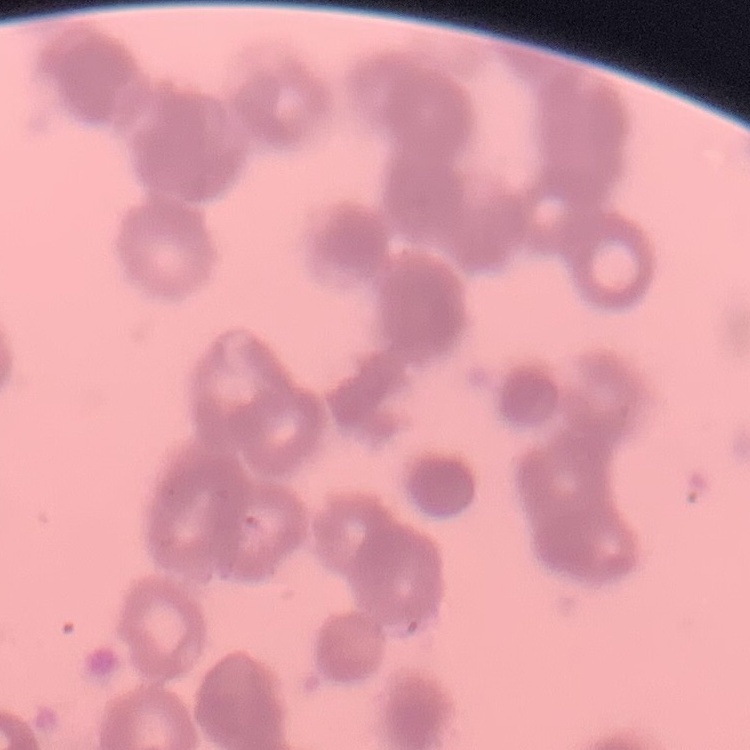

Summary:
  - Red blood cell morphology: rouleaux formation
  - Stain: Field's or Giemsa
  - Image type: one tile cut from a larger photomicrograph
  - Preparation: thin blood smear